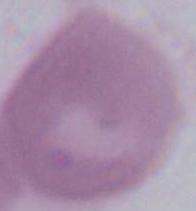
modality: micrograph
magnification: 1000x
identification: erythrocyte